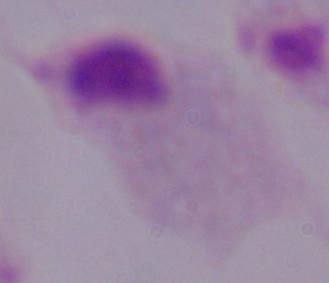

identification: trichomonad
modality: micrograph
magnification: 1000x